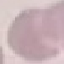

Result: no malaria parasites detected. Photographed with a smartphone camera at the microscope eyepiece. Automatically extracted cell patch, resized to 64 × 64 pixels. Thin blood film. Giemsa stain.